Name the blood parasite species.
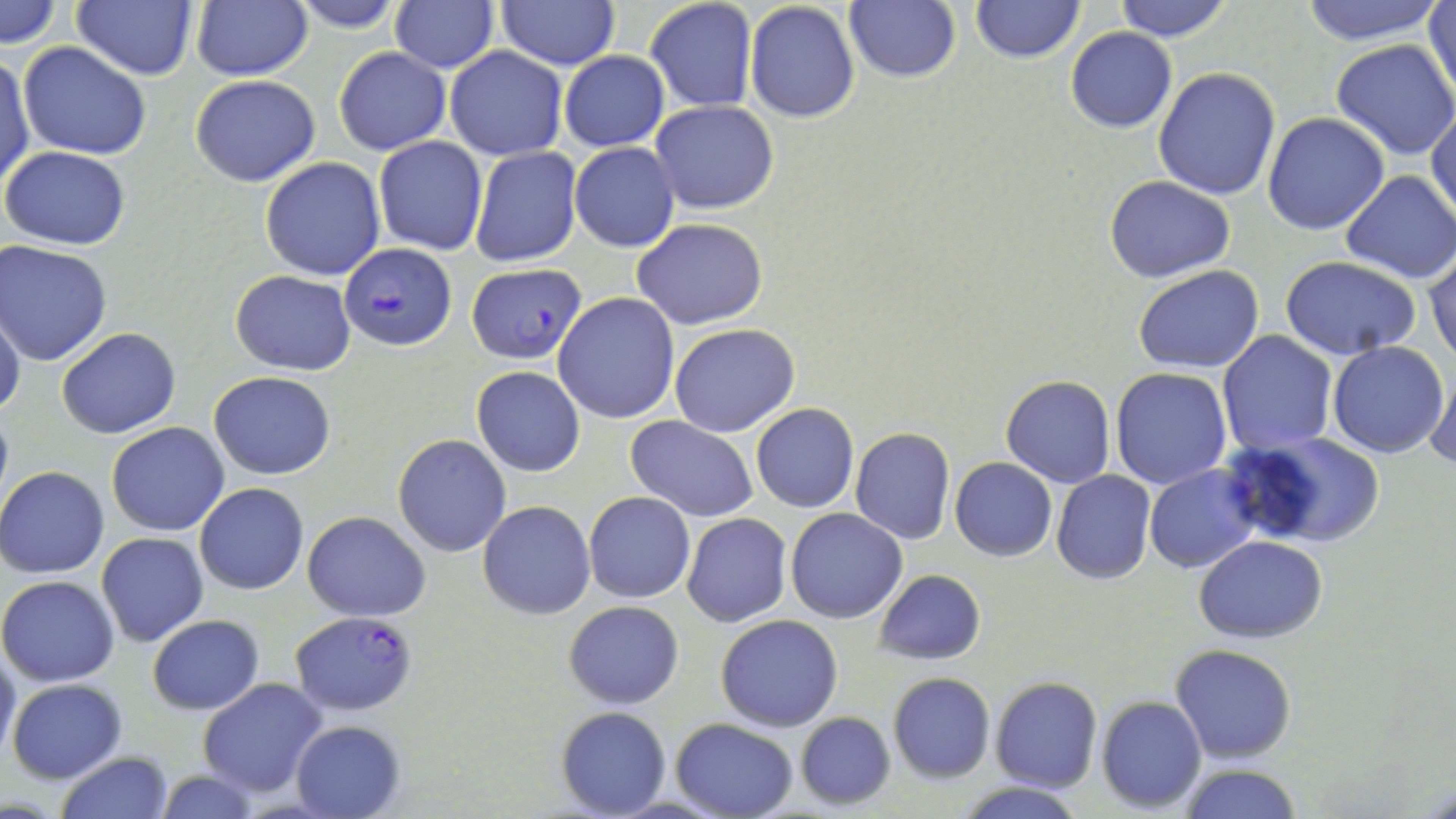

Plasmodium falciparum.

magnification = 1000x
stain = May-Grünwald-Giemsa
Plasmodium falciparum-infected red blood cell locations = approximate bounding boxes as (x1, y1, x2, y2) in pixels: (338, 242, 455, 351), (468, 262, 585, 365), (291, 611, 419, 715)
modality = light microscopy
preparation = thin blood smear
field of view = one of a larger specimen
image size = 1456×819 pixels
uninfected red blood cell locations = approximate bounding boxes as (x1, y1, x2, y2) in pixels: (1, 0, 62, 49), (73, 0, 197, 81), (189, 0, 311, 81), (287, 0, 406, 33), (644, 0, 758, 113), (844, 0, 961, 83), (969, 0, 1085, 64), (1110, 0, 1238, 43), (1427, 0, 1456, 102), (389, 1, 499, 73), (496, 1, 620, 70), (743, 1, 861, 124), (1293, 1, 1450, 45), (1064, 27, 1177, 133), (1331, 39, 1456, 158), (19, 42, 151, 162), (444, 47, 567, 161), (334, 48, 449, 155), (560, 51, 668, 150), (0, 54, 35, 194), (1152, 67, 1281, 199), (190, 75, 322, 187), (650, 100, 779, 213), (1428, 104, 1456, 224), (1263, 112, 1390, 235), (374, 136, 489, 255), (569, 141, 679, 252), (469, 145, 583, 269), (2, 146, 131, 250), (260, 157, 386, 281), (1340, 171, 1456, 282), (1105, 176, 1236, 282), (632, 218, 768, 329), (0, 240, 112, 366), (1425, 249, 1456, 367), (1280, 257, 1425, 360), (1132, 264, 1265, 374), (230, 270, 356, 375), (552, 293, 679, 424), (0, 307, 25, 422), (669, 323, 800, 437), (56, 327, 180, 439), (1218, 331, 1338, 454), (1327, 341, 1449, 458), (1427, 366, 1455, 472), (471, 367, 586, 478), (1111, 367, 1232, 489), (210, 370, 335, 480), (1001, 375, 1115, 488), (751, 404, 859, 513), (626, 416, 760, 523), (105, 422, 230, 536), (849, 428, 956, 545), (1225, 431, 1386, 548), (392, 434, 511, 557), (949, 458, 1058, 560), (1143, 464, 1257, 573), (0, 465, 109, 578), (1052, 470, 1156, 584), (194, 483, 308, 595), (584, 492, 696, 604), (479, 501, 596, 619), (785, 508, 908, 623), (302, 511, 431, 622), (681, 513, 792, 626), (96, 531, 208, 647), (1195, 535, 1327, 641), (873, 570, 986, 664), (0, 574, 120, 686), (564, 601, 684, 709), (716, 614, 843, 731), (147, 615, 264, 714), (0, 643, 20, 765), (1169, 644, 1297, 765), (888, 673, 995, 782), (990, 677, 1102, 791), (196, 678, 330, 799), (6, 679, 126, 784), (1097, 696, 1207, 811), (555, 706, 672, 817), (794, 712, 895, 809), (671, 717, 799, 819), (292, 720, 407, 819), (55, 751, 175, 819), (1177, 764, 1304, 819), (151, 768, 261, 819), (952, 781, 1089, 819)